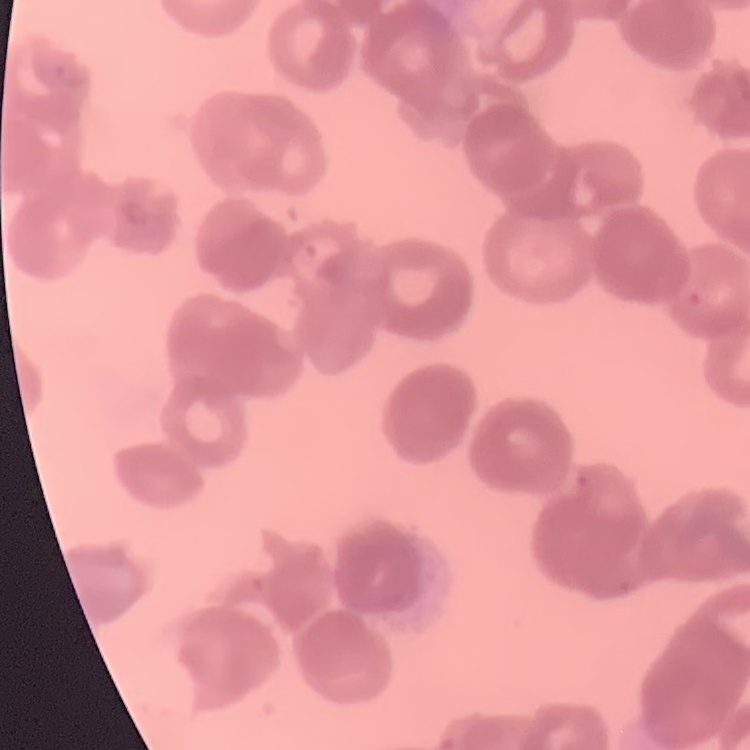

Summary:
  - Erythrocyte morphology: rouleaux formation
  - Image type: square crop of a larger photomicrograph
  - Stain: Field's or Giemsa
  - Preparation: thin blood film